State which parasite is depicted.
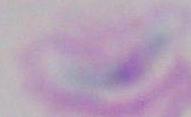
This is Toxoplasma gondii.

magnification = 1000x
modality = photomicrograph